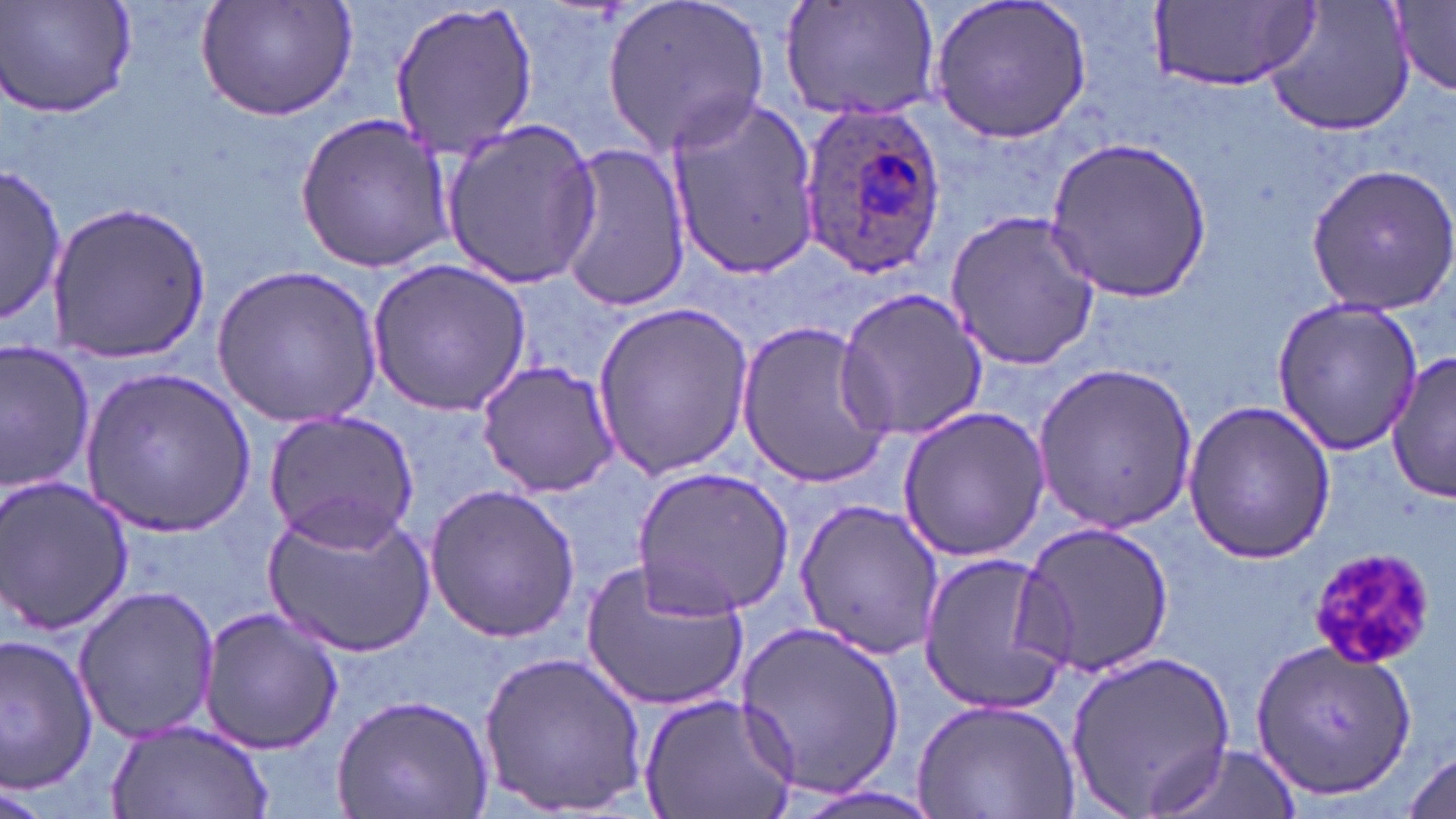
slide-level diagnosis = Plasmodium ovale
stain = May-Grünwald-Giemsa
uninfected red blood cell locations = approximate bounding boxes as named x1/y1/x2/y2 corners in pixels: (x1=3, y1=0, x2=138, y2=121), (x1=192, y1=0, x2=363, y2=122), (x1=603, y1=0, x2=771, y2=154), (x1=779, y1=0, x2=942, y2=124), (x1=928, y1=0, x2=1094, y2=147), (x1=1263, y1=0, x2=1415, y2=138), (x1=1393, y1=0, x2=1456, y2=98), (x1=387, y1=1, x2=536, y2=162), (x1=1152, y1=1, x2=1320, y2=92), (x1=666, y1=95, x2=822, y2=276), (x1=294, y1=109, x2=454, y2=273), (x1=439, y1=120, x2=602, y2=288), (x1=1046, y1=134, x2=1212, y2=301), (x1=548, y1=137, x2=693, y2=313), (x1=2, y1=164, x2=65, y2=325), (x1=1303, y1=164, x2=1456, y2=313), (x1=46, y1=200, x2=211, y2=363), (x1=943, y1=208, x2=1104, y2=372), (x1=365, y1=256, x2=531, y2=417), (x1=211, y1=264, x2=384, y2=425), (x1=836, y1=288, x2=991, y2=443), (x1=1270, y1=294, x2=1428, y2=459), (x1=591, y1=304, x2=753, y2=479), (x1=734, y1=319, x2=893, y2=484), (x1=0, y1=339, x2=97, y2=498), (x1=1386, y1=353, x2=1454, y2=506), (x1=1035, y1=359, x2=1200, y2=531), (x1=475, y1=360, x2=622, y2=498), (x1=80, y1=369, x2=255, y2=535), (x1=1180, y1=399, x2=1335, y2=566), (x1=898, y1=405, x2=1050, y2=564), (x1=263, y1=409, x2=421, y2=548), (x1=632, y1=467, x2=796, y2=618), (x1=0, y1=474, x2=133, y2=639), (x1=423, y1=484, x2=582, y2=641), (x1=792, y1=498, x2=943, y2=664), (x1=263, y1=502, x2=436, y2=661), (x1=1017, y1=520, x2=1175, y2=678), (x1=916, y1=549, x2=1072, y2=713), (x1=580, y1=556, x2=751, y2=714), (x1=72, y1=584, x2=223, y2=746), (x1=196, y1=604, x2=344, y2=756), (x1=733, y1=620, x2=906, y2=802), (x1=0, y1=632, x2=100, y2=794), (x1=1251, y1=639, x2=1417, y2=800), (x1=479, y1=648, x2=645, y2=816), (x1=1066, y1=649, x2=1238, y2=815), (x1=638, y1=691, x2=799, y2=819), (x1=334, y1=693, x2=492, y2=819), (x1=911, y1=698, x2=1080, y2=817), (x1=105, y1=719, x2=273, y2=819), (x1=1148, y1=743, x2=1298, y2=819), (x1=1400, y1=750, x2=1453, y2=817), (x1=1, y1=782, x2=48, y2=819)
image size = 1456×819 pixels
field of view = one of a larger specimen
platelet locations = approximate bounding boxes as named x1/y1/x2/y2 corners in pixels: (x1=1307, y1=544, x2=1440, y2=671)
modality = optical microscopy
preparation = thin blood film
Plasmodium ovale-infected red blood cell locations = approximate bounding boxes as named x1/y1/x2/y2 corners in pixels: (x1=793, y1=102, x2=946, y2=276)
magnification = 1000x